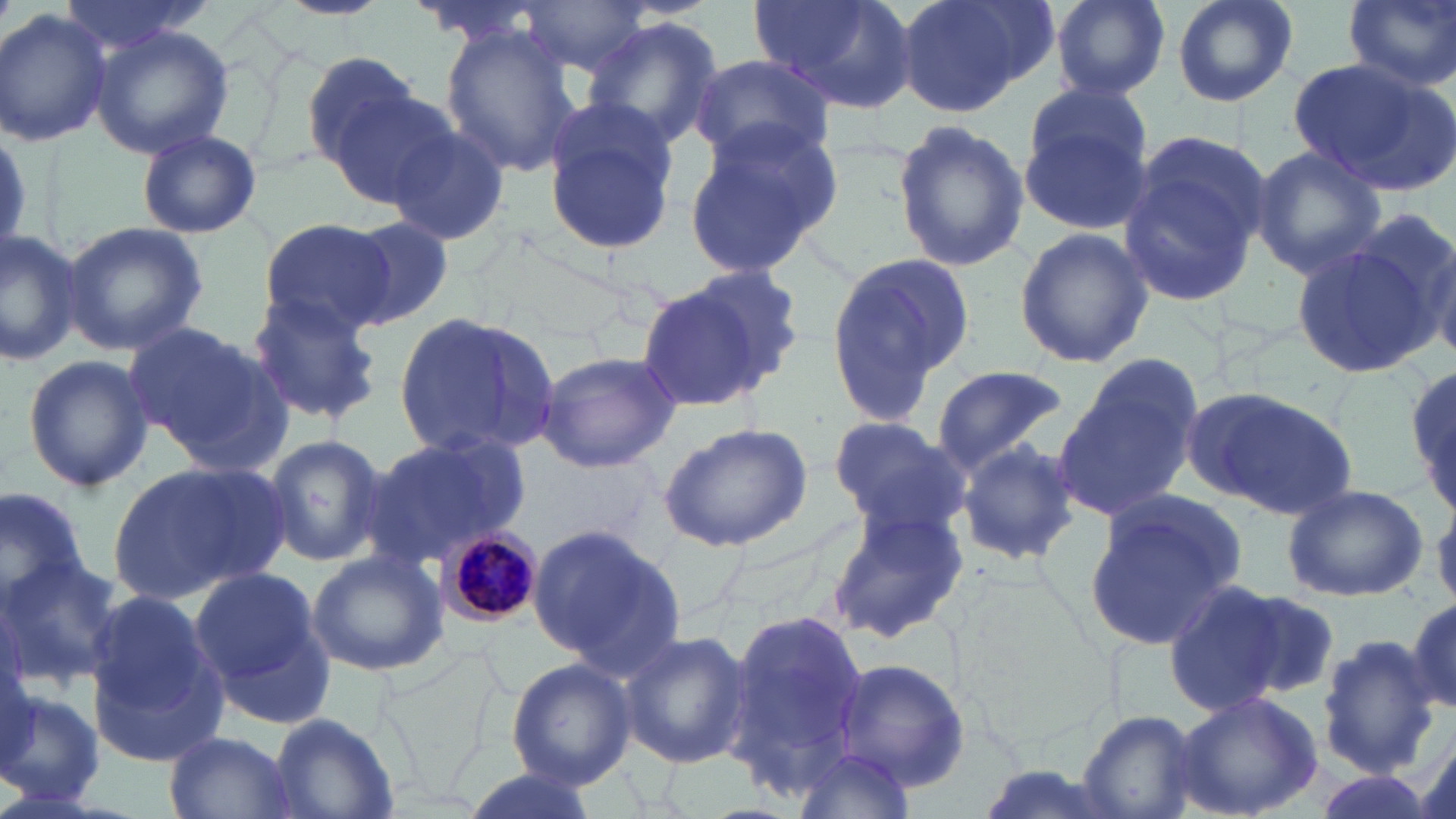

slide-level diagnosis = Plasmodium malariae
preparation = thin blood film
Plasmodium malariae-infected red blood cell locations = approximate bounding boxes as named x1/y1/x2/y2 corners in pixels: (x1=436, y1=522, x2=546, y2=628)
image size = 1456×819 pixels
modality = light microscopy
uninfected red blood cell locations = approximate bounding boxes as named x1/y1/x2/y2 corners in pixels: (x1=49, y1=0, x2=217, y2=60), (x1=280, y1=0, x2=387, y2=20), (x1=755, y1=0, x2=920, y2=116), (x1=895, y1=0, x2=1051, y2=118), (x1=1053, y1=0, x2=1170, y2=99), (x1=1170, y1=0, x2=1300, y2=108), (x1=1343, y1=0, x2=1456, y2=92), (x1=518, y1=1, x2=652, y2=77), (x1=1, y1=9, x2=112, y2=148), (x1=581, y1=17, x2=722, y2=149), (x1=87, y1=24, x2=236, y2=160), (x1=439, y1=27, x2=583, y2=178), (x1=298, y1=51, x2=421, y2=168), (x1=690, y1=52, x2=837, y2=164), (x1=1287, y1=57, x2=1453, y2=195), (x1=317, y1=76, x2=455, y2=206), (x1=1016, y1=84, x2=1158, y2=233), (x1=541, y1=106, x2=681, y2=259), (x1=890, y1=118, x2=1028, y2=275), (x1=681, y1=119, x2=843, y2=279), (x1=384, y1=123, x2=512, y2=246), (x1=136, y1=129, x2=262, y2=238), (x1=1119, y1=132, x2=1273, y2=309), (x1=1248, y1=144, x2=1388, y2=280), (x1=1345, y1=206, x2=1456, y2=355), (x1=259, y1=217, x2=399, y2=340), (x1=339, y1=218, x2=454, y2=330), (x1=63, y1=221, x2=208, y2=356), (x1=0, y1=225, x2=83, y2=363), (x1=1013, y1=228, x2=1153, y2=367), (x1=1289, y1=233, x2=1440, y2=384), (x1=823, y1=249, x2=976, y2=430), (x1=676, y1=261, x2=810, y2=386), (x1=632, y1=275, x2=780, y2=416), (x1=248, y1=294, x2=383, y2=423), (x1=393, y1=311, x2=562, y2=462), (x1=124, y1=321, x2=285, y2=464), (x1=535, y1=349, x2=680, y2=474), (x1=22, y1=352, x2=153, y2=493), (x1=1054, y1=360, x2=1201, y2=523), (x1=930, y1=365, x2=1069, y2=480), (x1=1409, y1=366, x2=1456, y2=517), (x1=1179, y1=383, x2=1359, y2=521), (x1=828, y1=416, x2=969, y2=532), (x1=660, y1=420, x2=814, y2=552), (x1=260, y1=433, x2=387, y2=569), (x1=364, y1=434, x2=527, y2=566), (x1=957, y1=437, x2=1082, y2=566), (x1=109, y1=461, x2=285, y2=602), (x1=0, y1=482, x2=90, y2=609), (x1=1282, y1=484, x2=1428, y2=602), (x1=1082, y1=496, x2=1243, y2=653), (x1=826, y1=499, x2=972, y2=642), (x1=528, y1=522, x2=685, y2=676), (x1=306, y1=551, x2=447, y2=678), (x1=0, y1=556, x2=127, y2=685), (x1=189, y1=567, x2=327, y2=715), (x1=1161, y1=578, x2=1290, y2=717), (x1=1228, y1=586, x2=1343, y2=703), (x1=1405, y1=594, x2=1456, y2=717), (x1=82, y1=595, x2=228, y2=765), (x1=720, y1=606, x2=876, y2=794), (x1=617, y1=631, x2=750, y2=767), (x1=1315, y1=634, x2=1441, y2=778), (x1=836, y1=655, x2=971, y2=793), (x1=506, y1=658, x2=636, y2=789), (x1=0, y1=687, x2=104, y2=806), (x1=1169, y1=690, x2=1325, y2=819), (x1=1076, y1=711, x2=1202, y2=819), (x1=269, y1=713, x2=399, y2=818), (x1=164, y1=730, x2=295, y2=819), (x1=788, y1=747, x2=920, y2=817), (x1=455, y1=769, x2=602, y2=819), (x1=1305, y1=772, x2=1436, y2=819)
magnification = 1000x
stain = May-Grünwald-Giemsa
field of view = one of a larger specimen